Name the parasite shown.
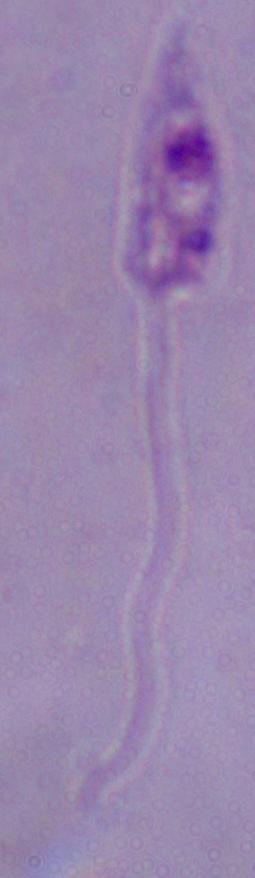

This is Leishmania.

magnification = 1000x
modality = photomicrograph